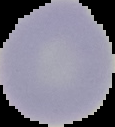
Summary:
  - Image size: 115×127 pixels
  - Malaria status: uninfected
  - Preparation: thin blood film
  - Image type: cell region segmented out of the field of view; surrounding area masked to black